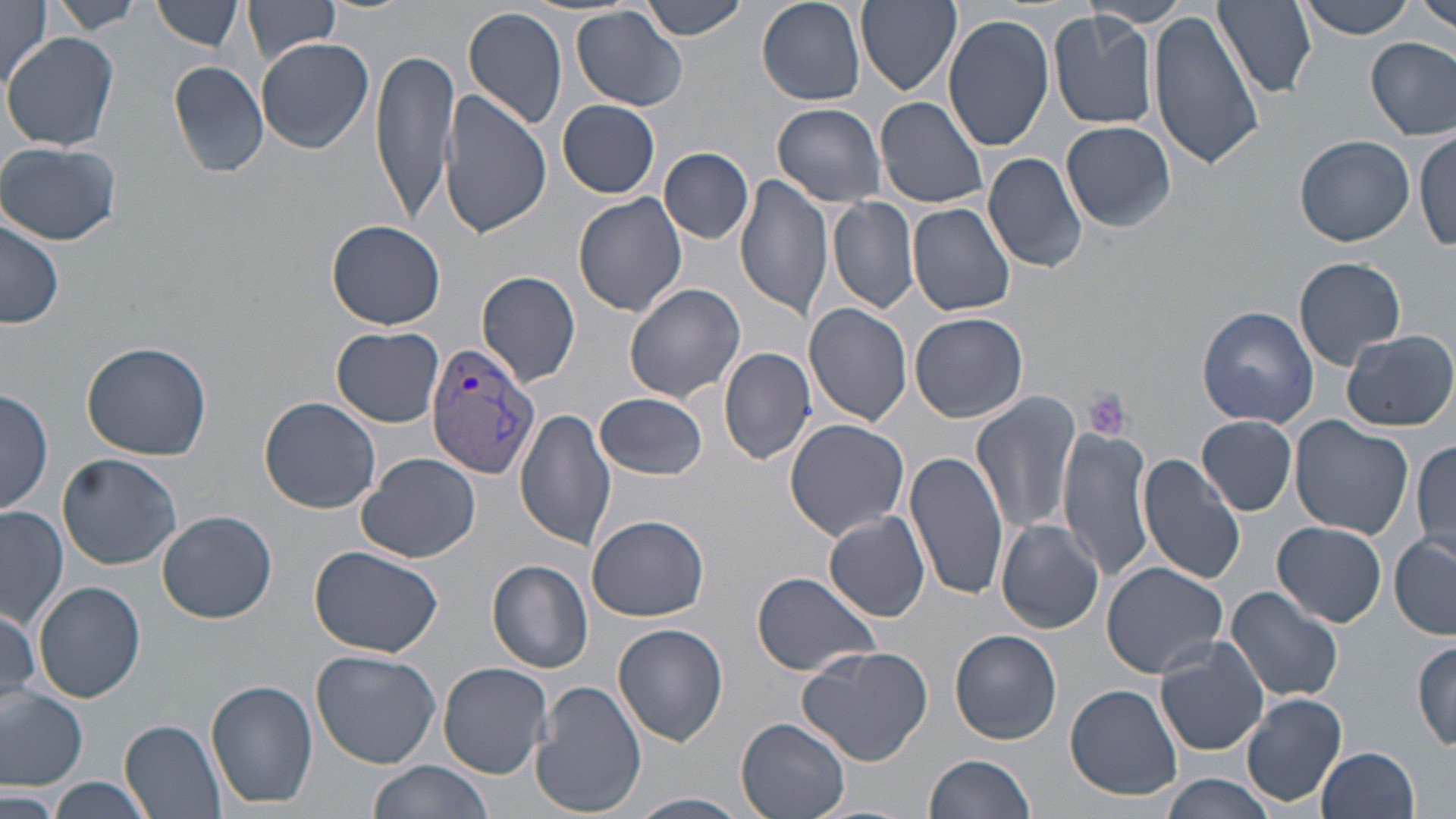
slide-level diagnosis = Plasmodium vivax
field of view = single
Plasmodium vivax-infected red blood cell locations = approximate bounding boxes as [x1, y1, x2, y2] in pixels: [424, 341, 541, 479]
stain = May-Grünwald-Giemsa
uninfected red blood cell locations = approximate bounding boxes as [x1, y1, x2, y2] in pixels: [45, 0, 146, 34], [153, 0, 244, 53], [638, 0, 750, 41], [756, 0, 864, 106], [855, 0, 963, 97], [1215, 0, 1315, 95], [1298, 0, 1420, 39], [1420, 0, 1456, 36], [0, 1, 54, 90], [244, 1, 340, 63], [1086, 1, 1192, 27], [1147, 5, 1264, 171], [462, 6, 568, 131], [572, 6, 689, 110], [1046, 11, 1160, 131], [943, 15, 1053, 151], [4, 32, 119, 150], [1366, 36, 1455, 139], [258, 38, 373, 152], [370, 48, 458, 221], [167, 58, 271, 178], [441, 92, 553, 239], [875, 96, 990, 209], [557, 99, 661, 198], [771, 102, 887, 206], [1061, 120, 1176, 232], [1413, 129, 1455, 252], [1295, 134, 1415, 246], [1, 142, 120, 246], [660, 147, 753, 243], [983, 151, 1089, 275], [735, 174, 833, 320], [574, 192, 688, 317], [826, 197, 919, 313], [908, 202, 1016, 316], [0, 216, 64, 330], [328, 219, 446, 328], [1294, 256, 1406, 369], [476, 271, 583, 388], [623, 283, 748, 404], [806, 303, 914, 427], [1197, 305, 1319, 428], [909, 312, 1029, 423], [332, 326, 445, 427], [1342, 330, 1455, 431], [81, 341, 215, 461], [719, 347, 818, 466], [0, 388, 52, 519], [596, 390, 708, 481], [971, 392, 1083, 538], [259, 396, 382, 513], [515, 409, 617, 549], [1197, 416, 1297, 515], [1289, 417, 1413, 539], [785, 418, 912, 540], [1057, 427, 1156, 582], [1412, 438, 1456, 558], [904, 451, 1010, 602], [58, 452, 181, 569], [358, 452, 479, 564], [1137, 453, 1246, 586], [1, 507, 67, 628], [157, 510, 277, 623], [588, 513, 710, 621], [823, 513, 931, 622], [996, 519, 1103, 634], [1273, 521, 1387, 627], [1389, 533, 1456, 638], [308, 546, 443, 657], [488, 560, 593, 672], [1101, 561, 1229, 680], [751, 572, 881, 677], [33, 580, 146, 703], [1227, 587, 1343, 705], [1, 601, 41, 706], [613, 623, 728, 746], [950, 630, 1060, 745], [1153, 636, 1271, 755], [1413, 638, 1455, 751], [796, 645, 932, 767], [310, 650, 441, 768], [439, 662, 551, 776], [530, 679, 647, 817], [207, 681, 318, 810], [1065, 684, 1182, 802], [0, 685, 88, 789], [1242, 692, 1348, 809], [736, 718, 851, 819], [120, 720, 227, 819], [1318, 747, 1421, 819], [925, 754, 1037, 819], [366, 758, 494, 818], [1159, 774, 1276, 819], [49, 778, 148, 819], [0, 786, 60, 817], [630, 793, 751, 819]
preparation = thin blood film
platelet locations = approximate bounding boxes as [x1, y1, x2, y2] in pixels: [1082, 387, 1133, 442]
magnification = 1000x
image size = 1456×819 pixels
modality = light microscopy